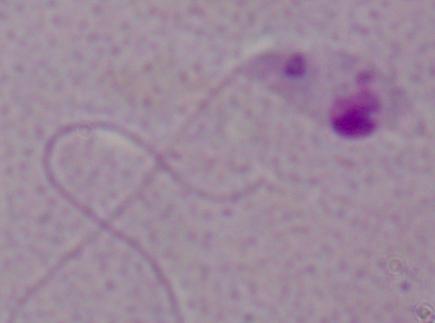
Summary:
  - Identification: Leishmania
  - Modality: micrograph
  - Magnification: 1000x